Assess the morphology of the red blood cells.
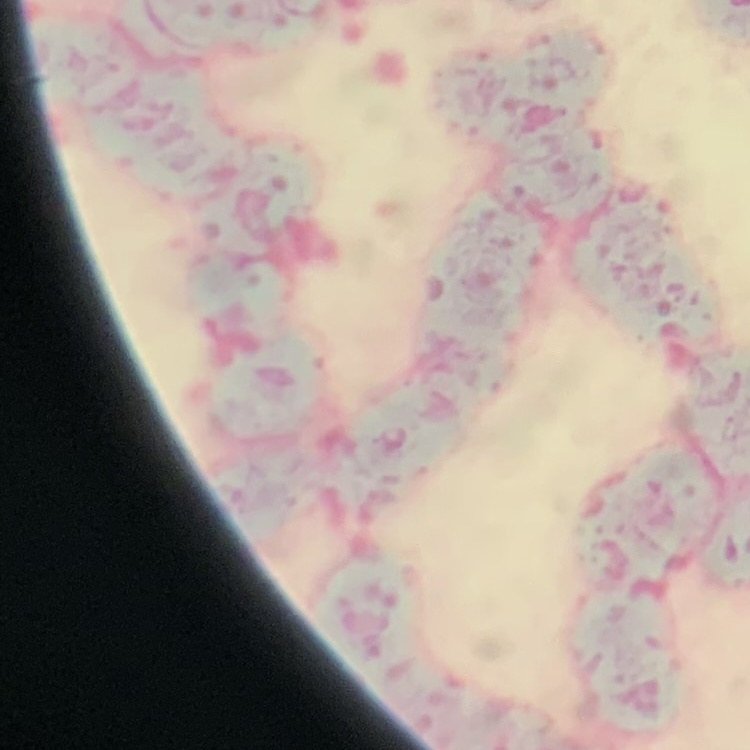
Rouleaux formation.

Field's or Giemsa stain. One tile cut from a larger photomicrograph. Thin blood smear.